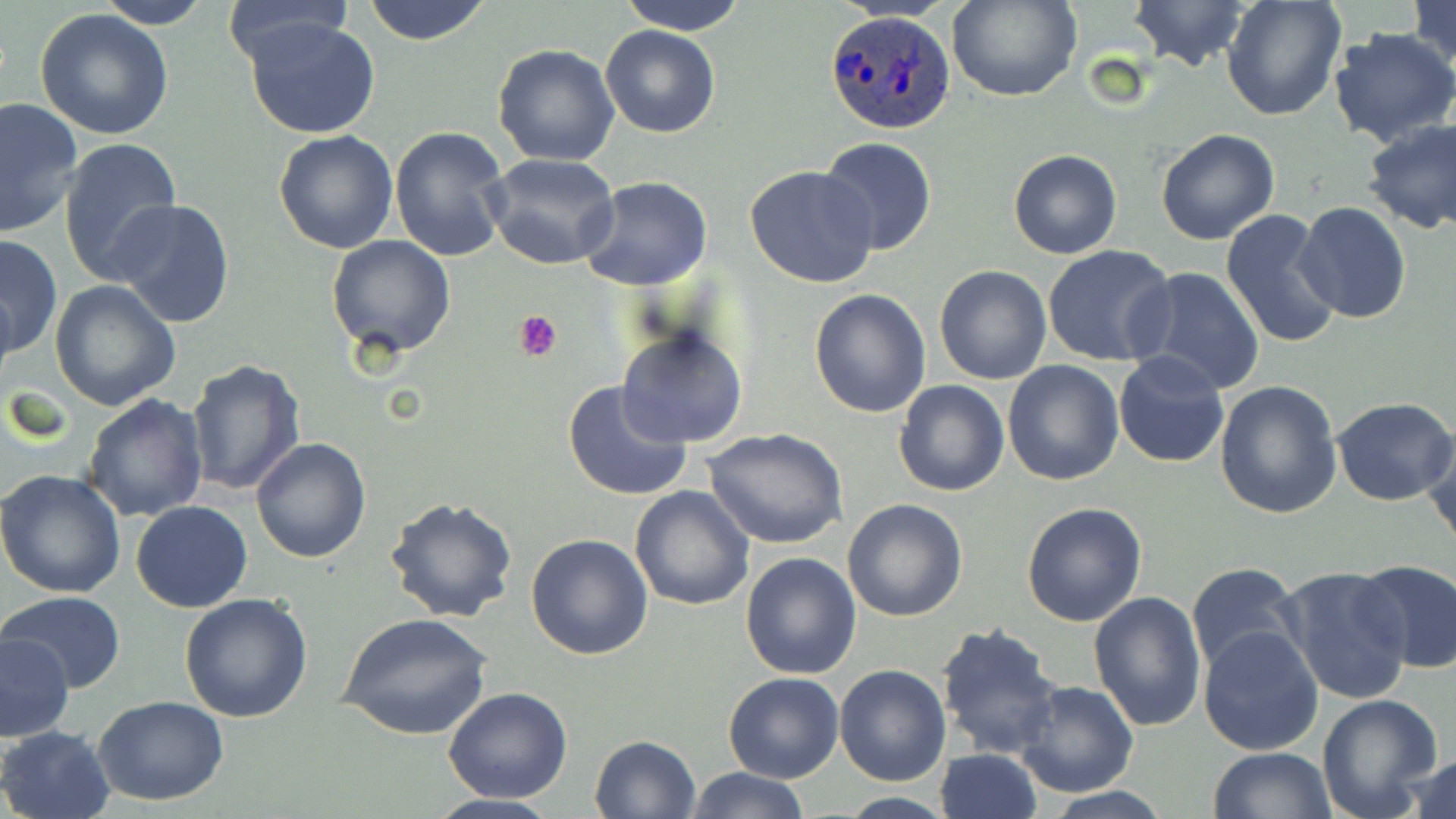
{
  "slide_level_diagnosis": "Plasmodium ovale",
  "uninfected_red_blood_cell_locations": "approximate bounding boxes as named x1/y1/x2/y2 corners in pixels: (x1=362, y1=0, x2=494, y2=46), (x1=616, y1=0, x2=749, y2=35), (x1=948, y1=0, x2=1080, y2=103), (x1=1129, y1=0, x2=1249, y2=74), (x1=1408, y1=0, x2=1456, y2=73), (x1=94, y1=1, x2=211, y2=30), (x1=1221, y1=1, x2=1346, y2=120), (x1=218, y1=2, x2=353, y2=64), (x1=35, y1=9, x2=175, y2=141), (x1=244, y1=17, x2=380, y2=140), (x1=600, y1=24, x2=720, y2=138), (x1=1328, y1=28, x2=1456, y2=147), (x1=492, y1=44, x2=620, y2=166), (x1=0, y1=96, x2=84, y2=236), (x1=1361, y1=117, x2=1456, y2=234), (x1=388, y1=126, x2=512, y2=264), (x1=1155, y1=128, x2=1280, y2=246), (x1=273, y1=130, x2=399, y2=254), (x1=60, y1=136, x2=182, y2=286), (x1=820, y1=137, x2=938, y2=256), (x1=1007, y1=150, x2=1123, y2=259), (x1=486, y1=153, x2=621, y2=271), (x1=745, y1=164, x2=879, y2=288), (x1=578, y1=175, x2=713, y2=291), (x1=109, y1=198, x2=237, y2=330), (x1=1294, y1=201, x2=1413, y2=323), (x1=1220, y1=208, x2=1343, y2=349), (x1=1, y1=232, x2=62, y2=357), (x1=326, y1=234, x2=457, y2=360), (x1=1043, y1=244, x2=1177, y2=368), (x1=934, y1=265, x2=1051, y2=384), (x1=1128, y1=266, x2=1267, y2=398), (x1=50, y1=281, x2=182, y2=410), (x1=808, y1=288, x2=931, y2=417), (x1=616, y1=323, x2=748, y2=450), (x1=1114, y1=350, x2=1231, y2=467), (x1=186, y1=358, x2=308, y2=497), (x1=1003, y1=361, x2=1124, y2=484), (x1=563, y1=378, x2=695, y2=502), (x1=894, y1=379, x2=1009, y2=496), (x1=1214, y1=380, x2=1344, y2=520), (x1=81, y1=392, x2=208, y2=522), (x1=1331, y1=396, x2=1456, y2=506), (x1=703, y1=427, x2=849, y2=550), (x1=1420, y1=430, x2=1455, y2=547), (x1=250, y1=437, x2=372, y2=565), (x1=0, y1=469, x2=127, y2=596), (x1=629, y1=485, x2=756, y2=611), (x1=385, y1=495, x2=519, y2=623), (x1=842, y1=499, x2=968, y2=622), (x1=131, y1=501, x2=253, y2=613), (x1=1021, y1=501, x2=1149, y2=627), (x1=525, y1=534, x2=653, y2=661), (x1=739, y1=551, x2=863, y2=680), (x1=1353, y1=559, x2=1456, y2=673), (x1=1185, y1=562, x2=1303, y2=679), (x1=1275, y1=565, x2=1415, y2=707), (x1=1087, y1=591, x2=1207, y2=732), (x1=3, y1=593, x2=127, y2=692), (x1=179, y1=593, x2=315, y2=723), (x1=339, y1=611, x2=493, y2=740), (x1=935, y1=621, x2=1064, y2=760), (x1=1198, y1=625, x2=1325, y2=755), (x1=1, y1=634, x2=73, y2=741), (x1=835, y1=664, x2=952, y2=786), (x1=723, y1=673, x2=845, y2=784), (x1=1015, y1=680, x2=1139, y2=796), (x1=443, y1=687, x2=573, y2=803), (x1=1316, y1=694, x2=1443, y2=819), (x1=95, y1=695, x2=229, y2=805), (x1=0, y1=725, x2=115, y2=819), (x1=589, y1=735, x2=701, y2=819), (x1=935, y1=748, x2=1042, y2=819), (x1=1206, y1=748, x2=1334, y2=819), (x1=1403, y1=752, x2=1455, y2=819), (x1=686, y1=766, x2=807, y2=819), (x1=421, y1=793, x2=567, y2=819), (x1=834, y1=793, x2=958, y2=819)",
  "plasmodium_ovale_infected_red_blood_cell_locations": "approximate bounding boxes as named x1/y1/x2/y2 corners in pixels: (x1=824, y1=9, x2=955, y2=134)",
  "field_of_view": "one of a larger specimen",
  "magnification": "1000x",
  "image_size": "1456×819 pixels",
  "stain": "May-Grünwald-Giemsa",
  "modality": "optical microscopy",
  "preparation": "thin blood film",
  "platelet_locations": "approximate bounding boxes as named x1/y1/x2/y2 corners in pixels: (x1=514, y1=309, x2=563, y2=361)"
}